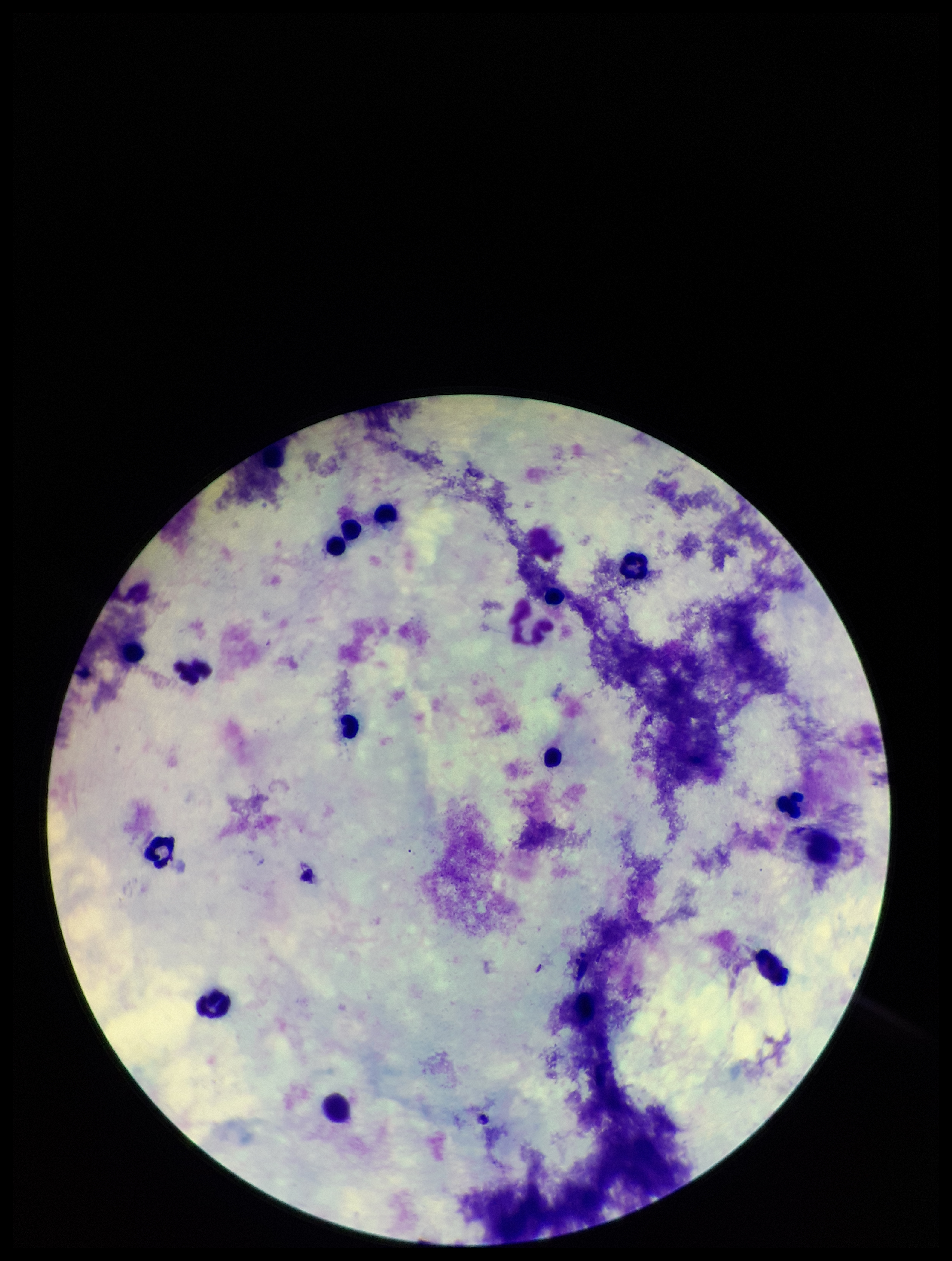
patient_malaria_status: negative
parasite_count: 0
capture: smartphone photograph through the microscope eyepiece
stain: Giemsa
field_of_view: single
preparation: thick blood smear
image_size: 952×1261 pixels
plasmodium_parasites: none seen
leukocyte_count: 14